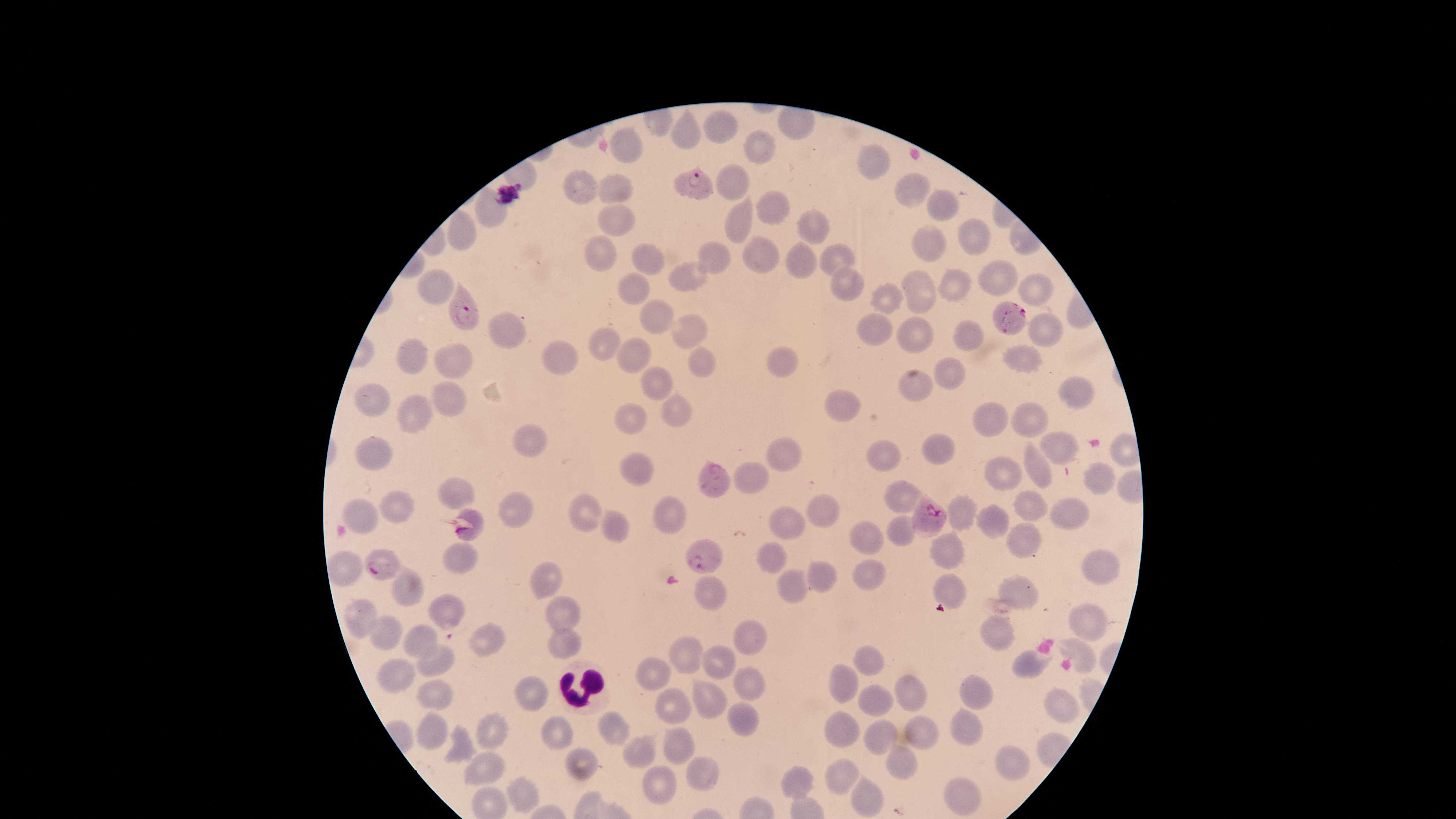

Approximate marker points as (x, y) in pixels. Uninfected red blood cells: (714, 128), (688, 129), (758, 147), (630, 154), (869, 157), (729, 182), (590, 188), (617, 189), (913, 190), (940, 200), (778, 207), (492, 209), (617, 221), (741, 221), (815, 226), (460, 232), (975, 238), (922, 247), (601, 248), (765, 254), (643, 256), (835, 257), (713, 258), (802, 260), (995, 276), (686, 278), (915, 278), (637, 282), (847, 282), (437, 284), (1028, 284), (959, 285), (888, 296), (921, 297), (653, 319), (1046, 327), (872, 328), (504, 331), (908, 331), (690, 333), (971, 335), (599, 341), (635, 354), (409, 355), (559, 358), (1023, 358), (781, 363), (454, 364), (701, 364), (954, 375), (654, 383), (913, 385), (453, 389), (1077, 394), (373, 404), (674, 411), (843, 411), (425, 415), (1031, 417), (991, 419), (628, 420), (534, 440), (940, 446), (1061, 449), (882, 451), (369, 452), (786, 452), (635, 467), (1037, 467), (756, 473), (1002, 474), (1093, 479), (451, 491), (901, 493), (1028, 504), (815, 505), (400, 508), (521, 508), (356, 511), (668, 512), (964, 513), (1066, 513), (587, 514), (785, 517), (999, 522), (616, 528), (903, 530), (871, 534), (1024, 540), (458, 553), (949, 553), (774, 558), (1101, 564), (345, 566), (874, 575), (819, 578), (543, 579), (1016, 585), (949, 586), (411, 589), (790, 590), (707, 591), (446, 608), (569, 612), (362, 620), (1091, 622), (391, 630), (996, 632), (751, 633), (420, 636), (485, 638), (569, 638), (1076, 649), (685, 650), (1023, 658), (718, 659), (869, 659), (439, 660), (401, 668), (653, 673), (840, 677), (745, 678), (438, 691), (535, 691), (905, 692), (981, 692), (705, 699), (875, 699), (676, 702), (1060, 704), (745, 718), (966, 724), (434, 727), (844, 727), (919, 727), (487, 729), (614, 730), (876, 735), (556, 736), (454, 744), (676, 746), (643, 755), (908, 759), (1011, 760), (579, 764), (703, 769), (490, 770), (840, 770), (661, 783), (796, 783), (525, 793), (957, 796), (867, 798). White blood cells: (578, 685). Parasitized red blood cells: (689, 182), (463, 315), (1009, 316), (715, 479), (924, 516), (468, 526), (699, 556), (381, 563). Thin smear of blood. Single field of view. Species: Plasmodium falciparum. Giemsa-stained preparation. Photographed with a smartphone camera through the microscope eyepiece. Presence: malaria parasites identified. The visible region is circular. Image is 1456×819 pixels.